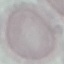

malaria_status: uninfected
image_type: cell patch, automatically extracted from a larger field of view and resized to 64 × 64 pixels
stain: Giemsa
preparation: thin blood film
capture: smartphone through the microscope eyepiece